Assess this cell for malaria.
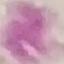
Uninfected.

stain = Giemsa
capture = smartphone through the microscope eyepiece
image type = cell patch, automatically extracted from a larger field of view and resized to 64 × 64 pixels
preparation = thin blood smear